Give the extent of all uninfected red blood cells.
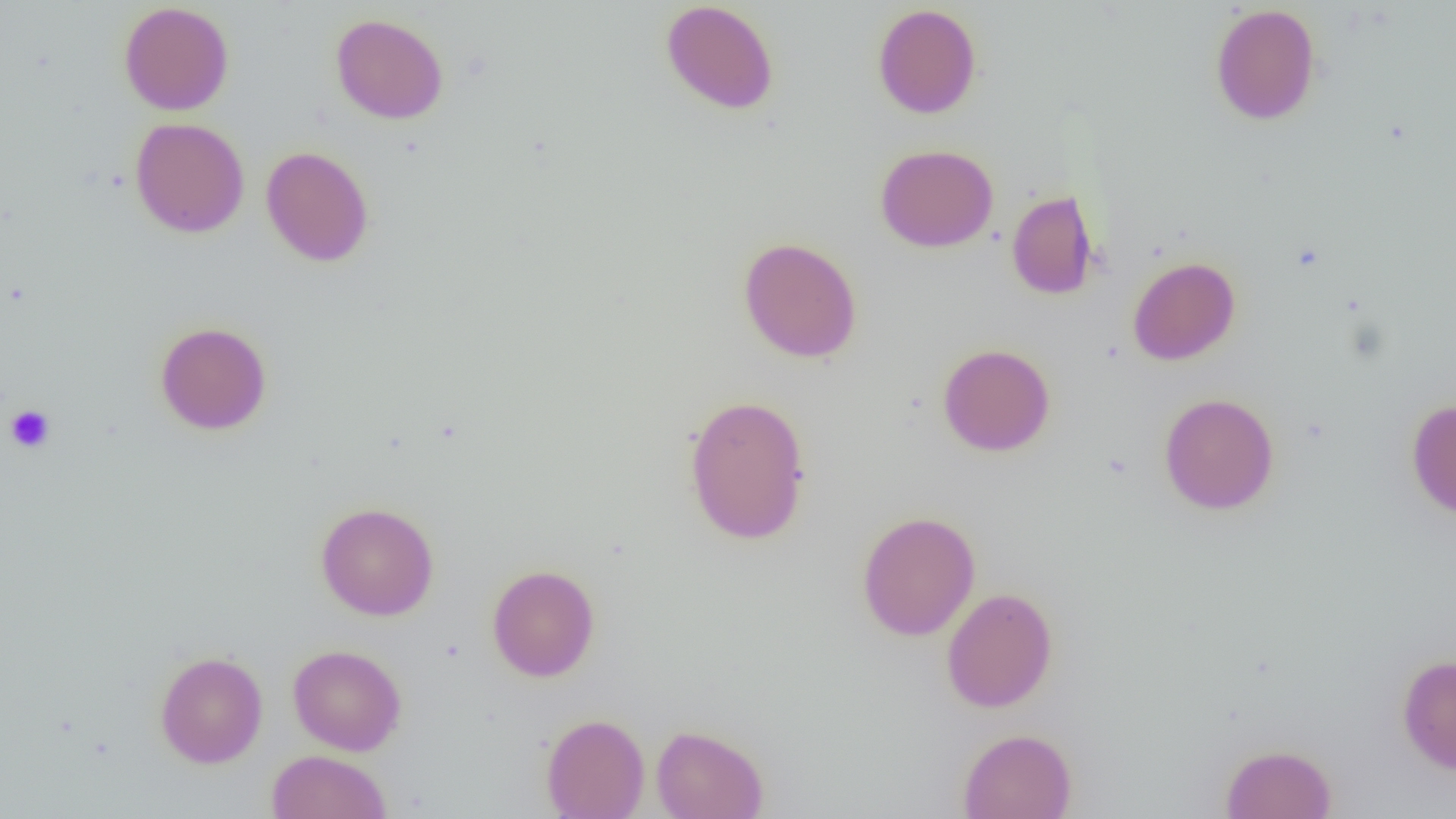
Approximate bounding boxes as named x1/y1/x2/y2 corners in pixels.
Uninfected red blood cells: (x1=660, y1=0, x2=779, y2=115), (x1=119, y1=2, x2=234, y2=115), (x1=872, y1=3, x2=982, y2=119), (x1=1209, y1=3, x2=1322, y2=126), (x1=331, y1=13, x2=448, y2=124), (x1=130, y1=117, x2=249, y2=238), (x1=875, y1=144, x2=998, y2=252), (x1=261, y1=146, x2=374, y2=267), (x1=1006, y1=189, x2=1100, y2=300), (x1=738, y1=236, x2=862, y2=363), (x1=1127, y1=256, x2=1240, y2=365), (x1=155, y1=321, x2=272, y2=435), (x1=937, y1=343, x2=1055, y2=457), (x1=1158, y1=392, x2=1279, y2=515), (x1=683, y1=394, x2=812, y2=545), (x1=1406, y1=399, x2=1456, y2=519), (x1=315, y1=502, x2=439, y2=621), (x1=856, y1=510, x2=980, y2=641), (x1=486, y1=564, x2=600, y2=681), (x1=941, y1=587, x2=1058, y2=713), (x1=288, y1=644, x2=407, y2=756), (x1=154, y1=650, x2=268, y2=768), (x1=1396, y1=653, x2=1456, y2=773), (x1=541, y1=713, x2=650, y2=819), (x1=651, y1=724, x2=769, y2=819), (x1=957, y1=728, x2=1077, y2=819), (x1=1219, y1=743, x2=1337, y2=819), (x1=266, y1=750, x2=392, y2=819).

Platelet locations: (x1=5, y1=404, x2=55, y2=453). Slide-level diagnosis: no evidence of blood parasites. Image is 1456×819 pixels. Captured at 1000x magnification. One field of a larger specimen. Light microscopy. Thin blood smear.